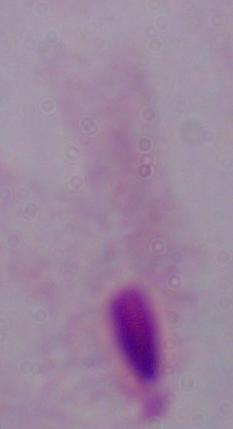

1000x magnification. Photomicrograph. A trichomonad is shown.